Locate platelets.
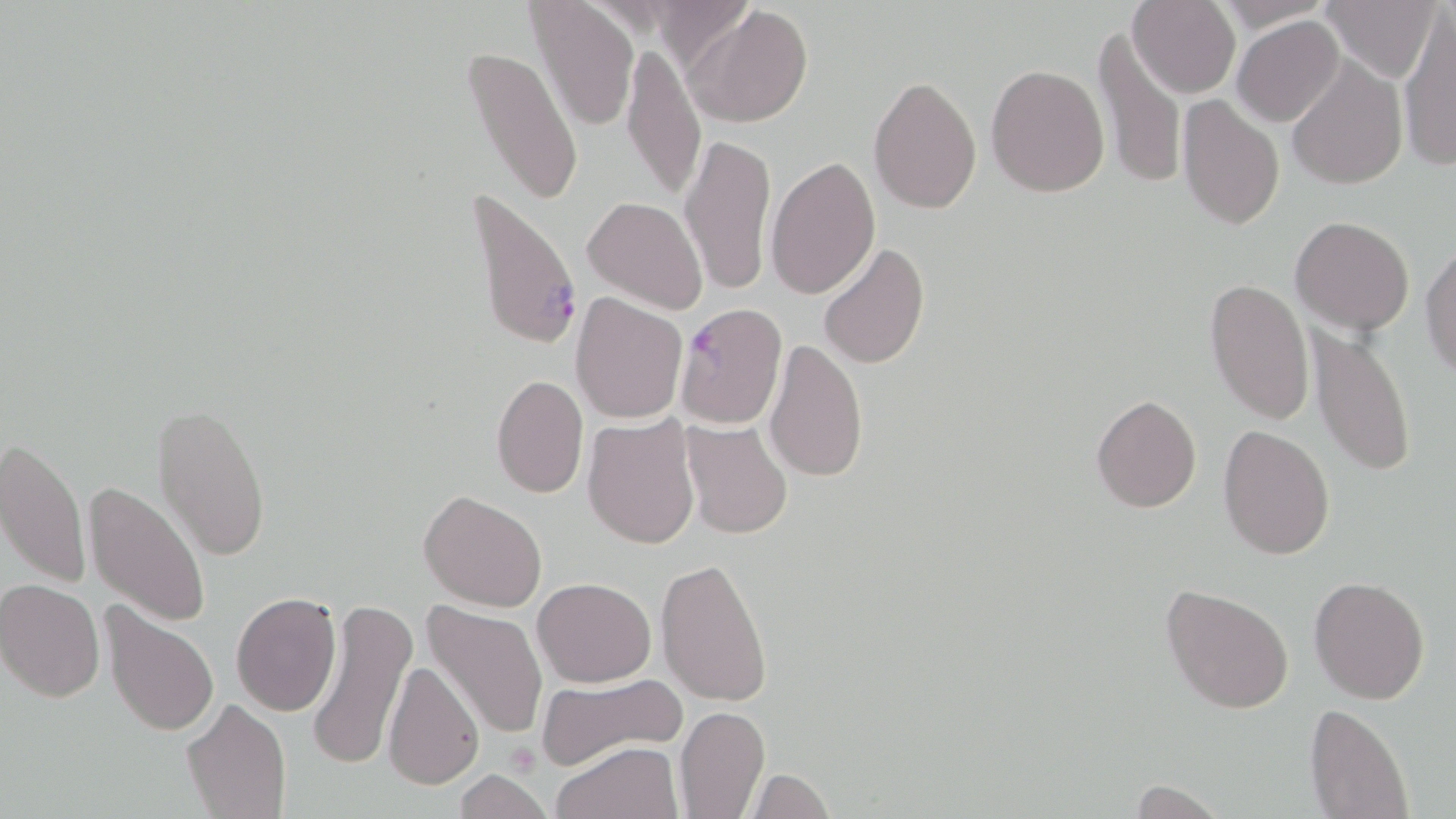

Approximate bounding boxes as (x1,y1)-(x2,y2) corner pairs in pixels.
Platelets: (504,742)-(540,775).

Plasmodium falciparum-infected red blood cell locations: (466,182)-(582,355), (674,301)-(789,431). Uninfected red blood cell locations: (1127,0)-(1239,98), (1213,0)-(1337,33), (1320,0)-(1441,83), (529,1)-(639,130), (685,5)-(814,127), (1397,11)-(1455,168), (1232,16)-(1343,126), (1093,27)-(1186,194), (621,38)-(707,206), (463,43)-(583,209), (1286,58)-(1407,191), (986,63)-(1110,197), (868,74)-(982,214), (1176,96)-(1285,230), (681,132)-(777,295), (766,155)-(881,299), (582,196)-(707,314), (1290,215)-(1415,335), (1421,238)-(1455,375), (817,242)-(930,370), (1204,278)-(1315,425), (570,293)-(687,425), (1306,326)-(1417,479), (763,337)-(868,482), (491,374)-(588,499), (1091,393)-(1202,513), (151,401)-(272,562), (581,415)-(701,549), (681,420)-(793,538), (1218,423)-(1335,559), (1,437)-(89,592), (85,480)-(213,629), (419,489)-(547,611), (655,556)-(773,705), (1309,575)-(1431,704), (533,577)-(656,687), (0,578)-(106,702), (1162,584)-(1294,715), (231,592)-(341,716), (98,598)-(219,738), (304,599)-(418,770), (420,600)-(548,742), (381,659)-(484,789), (536,673)-(687,769), (181,699)-(292,819), (1304,703)-(1414,819), (675,705)-(770,819), (551,740)-(681,819), (746,767)-(834,819), (454,769)-(552,819). Slide-level diagnosis: Plasmodium falciparum. 1000x magnification. Thin blood smear. Light microscopy. Image is 1456×819 pixels. One field of a larger specimen. May-Grünwald-Giemsa stain.